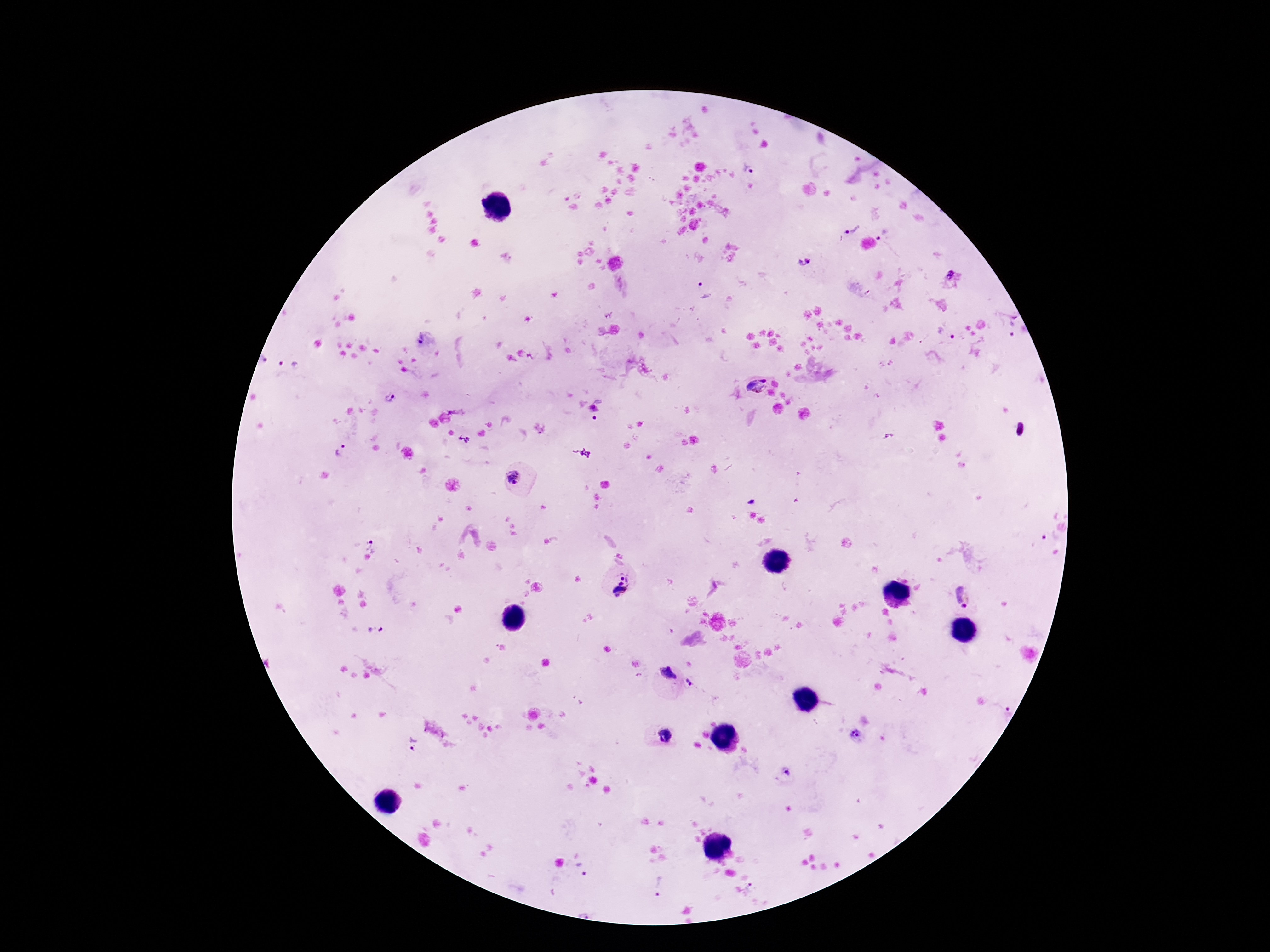
{
  "magnification": "100x",
  "image_size": "1270×952 pixels",
  "field_of_view": "single",
  "stain": "Giemsa",
  "plasmodium_parasite_locations": "approximate centers as {x, y} in pixels: {749, 168}, {853, 226}, {883, 234}, {805, 259}, {951, 276}, {703, 288}, {1007, 321}, {947, 332}, {422, 339}, {262, 360}, {288, 364}, {755, 385}, {390, 397}, {593, 409}, {456, 412}, {595, 419}, {465, 439}, {344, 450}, {513, 477}, {1050, 537}, {372, 545}, {621, 584}, {963, 597}, {375, 630}, {669, 674}, {691, 682}, {1008, 709}, {665, 734}, {856, 734}, {413, 744}, {786, 773}, {581, 869}, {660, 884}, {752, 891}, {586, 910}",
  "patient_malaria_status": "infected",
  "preparation": "thick blood smear",
  "capture": "smartphone camera through the microscope eyepiece"
}